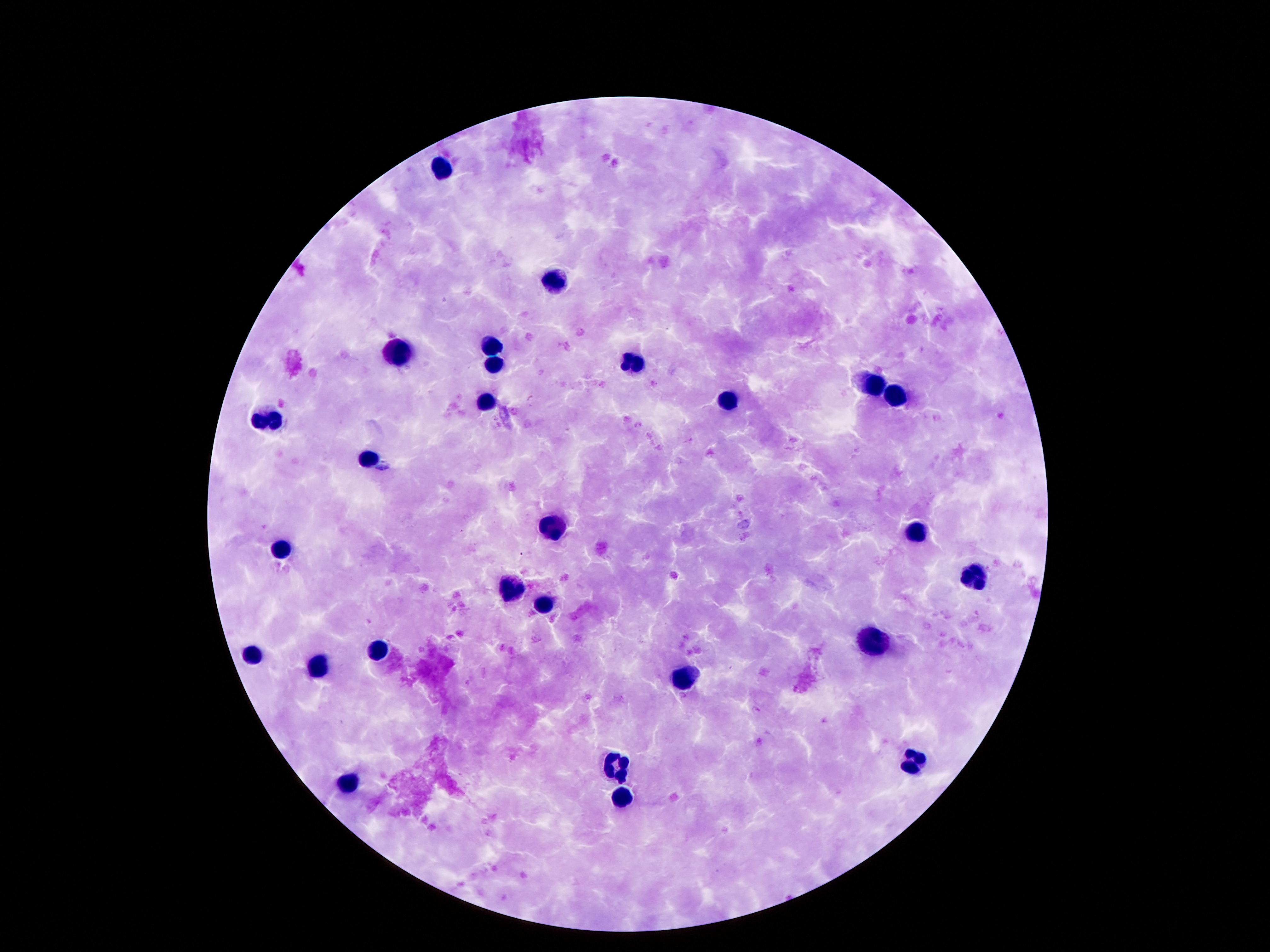
Approximate centers as (x, y) in pixels.
Summary:
  - Leukocyte locations: (442, 167), (556, 275), (492, 346), (397, 356), (493, 362), (636, 366), (872, 384), (896, 397), (728, 401), (486, 402), (268, 420), (368, 459), (552, 529), (915, 531), (281, 549), (973, 571), (508, 590), (545, 603), (874, 644), (379, 649), (252, 656), (322, 665), (683, 678), (915, 761), (619, 767), (347, 781), (624, 797)
  - Capture: smartphone camera through the microscope eyepiece
  - Magnification: 100x
  - Patient malaria status: uninfected
  - Preparation: thick blood smear
  - Field of view: one from this slide
  - Image size: 1270×952 pixels
  - Stain: Giemsa